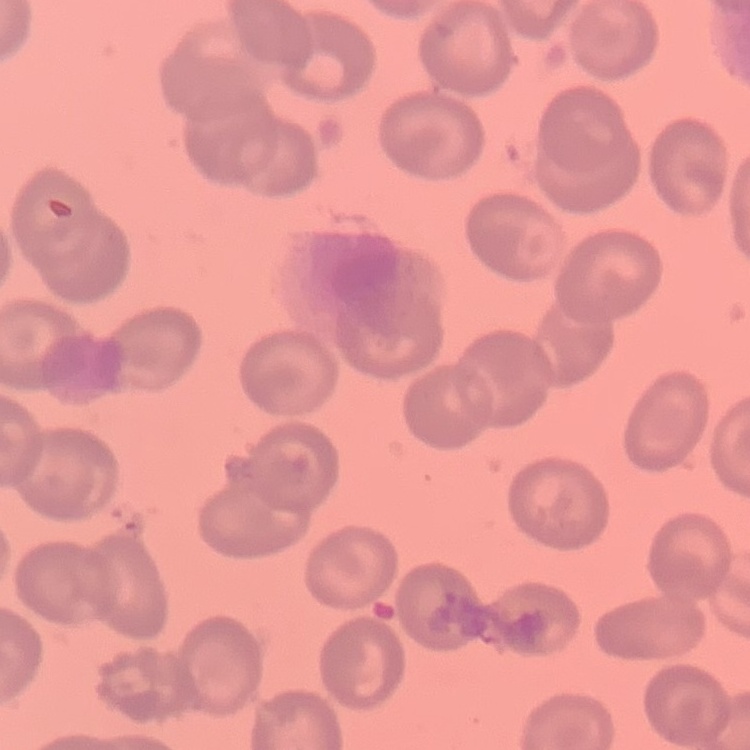 The erythrocytes exhibit no rouleaux formation. Square crop of a larger photomicrograph. Thin blood film. Field's or Giemsa stain.